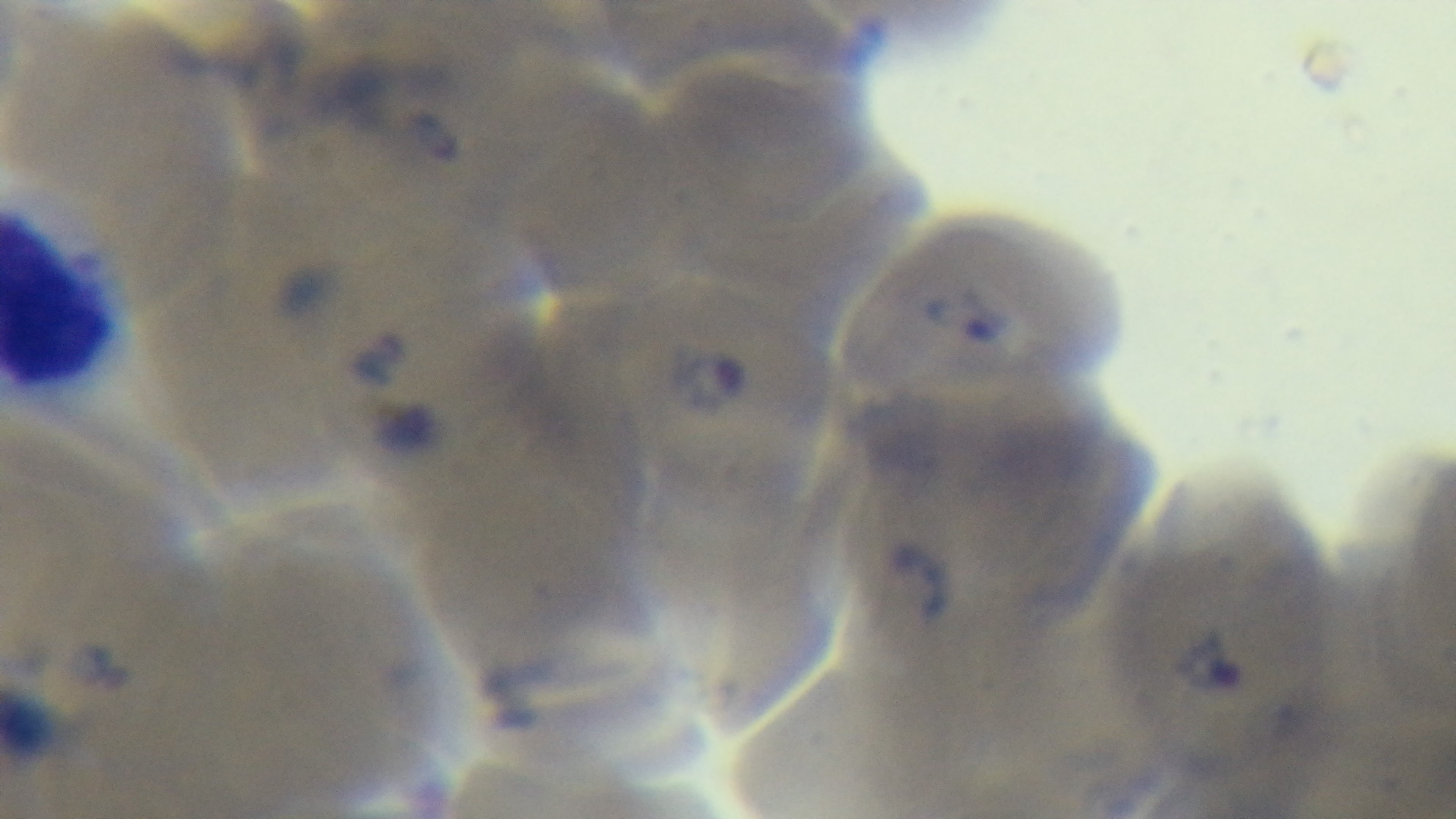

Giemsa stain. Light microscopy. Captured with a mounted 4K digital camera. 100x oil-immersion objective. Malaria status: infected. Preparation: thin. Single field of view.